Locate and identify every blood parasite.
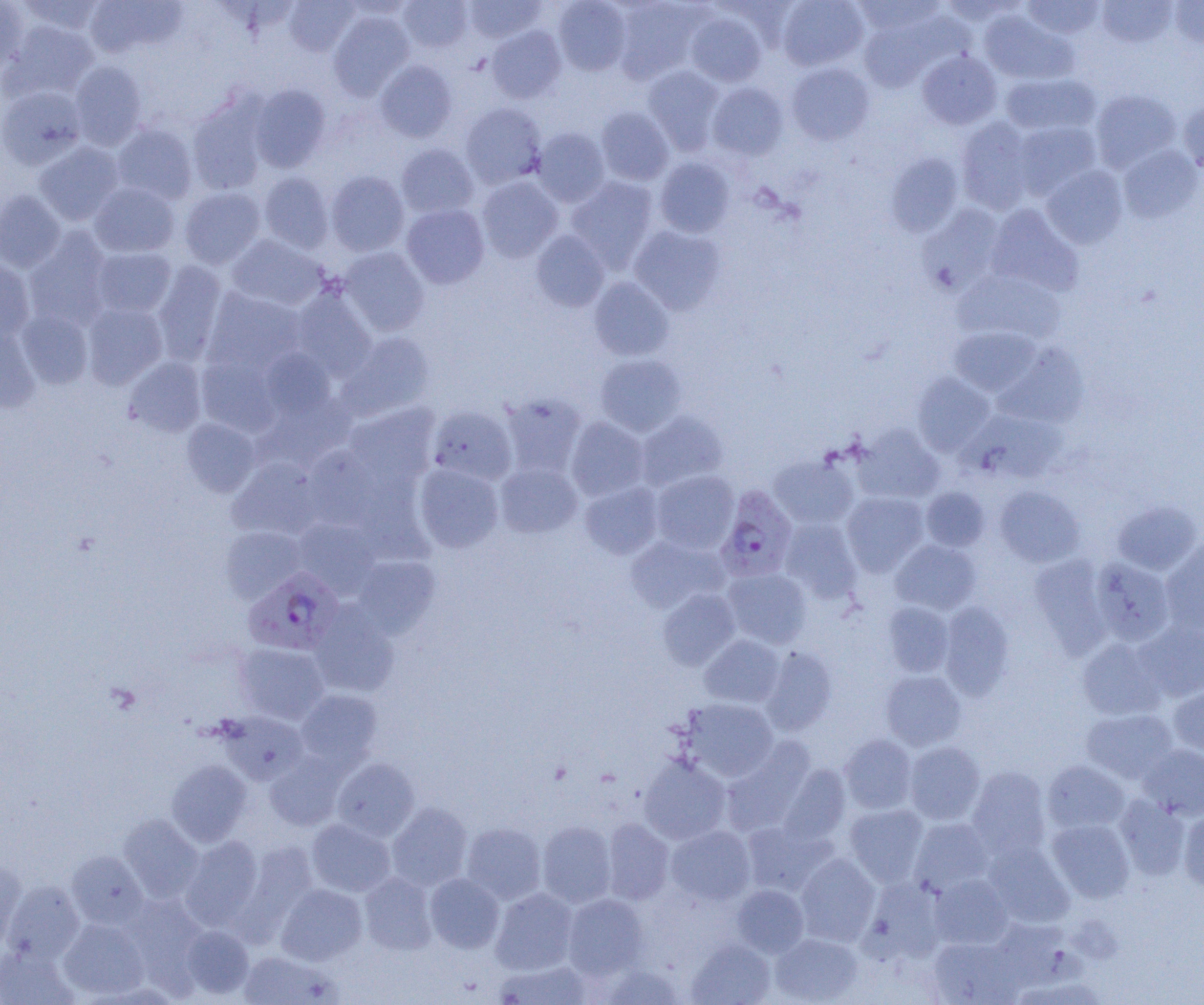

Approximate bounding boxes as (x1, y1, x2, y2) in pixels.
Plasmodium falciparum-infected red blood cells: (715, 485, 798, 582), (244, 567, 344, 654).
No Plasmodium ovale, Plasmodium malariae, Plasmodium vivax, Babesia divergens, or Trypanosoma brucei observed.

Uninfected red blood cell locations: (0, 0, 29, 75), (16, 0, 107, 37), (82, 0, 184, 58), (283, 0, 359, 55), (398, 0, 472, 52), (464, 0, 545, 43), (553, 0, 632, 75), (777, 0, 868, 71), (852, 0, 946, 35), (939, 0, 1025, 26), (1022, 0, 1104, 39), (1097, 0, 1177, 48), (612, 1, 706, 84), (1169, 1, 1204, 47), (685, 10, 767, 87), (329, 11, 414, 99), (979, 11, 1074, 84), (858, 17, 941, 92), (3, 20, 98, 100), (487, 26, 565, 103), (918, 50, 1001, 130), (375, 60, 456, 142), (69, 61, 147, 150), (786, 63, 874, 145), (642, 65, 725, 154), (1001, 72, 1100, 136), (707, 82, 788, 160), (249, 84, 331, 172), (0, 85, 88, 170), (1091, 89, 1181, 172), (188, 98, 269, 194), (1178, 98, 1204, 174), (460, 103, 547, 187), (595, 106, 674, 186), (956, 117, 1035, 215), (1012, 121, 1101, 199), (111, 123, 198, 205), (532, 127, 610, 207), (34, 142, 124, 226), (397, 144, 479, 219), (1118, 145, 1202, 223), (886, 153, 964, 238), (654, 157, 735, 238), (1041, 165, 1128, 249), (326, 171, 409, 256), (259, 172, 334, 253), (476, 176, 563, 262), (565, 176, 659, 271), (90, 182, 179, 258), (180, 186, 265, 269), (0, 190, 66, 272), (401, 204, 489, 289), (919, 204, 1007, 295), (986, 205, 1083, 296), (628, 224, 727, 314), (24, 230, 114, 330), (531, 230, 610, 311), (227, 234, 326, 311), (91, 247, 176, 318), (338, 247, 429, 336), (0, 258, 35, 344), (152, 260, 228, 363), (953, 269, 1065, 345), (589, 277, 674, 361), (290, 286, 377, 379), (203, 288, 304, 375), (82, 302, 168, 388), (16, 309, 93, 388), (948, 325, 1042, 397), (0, 327, 40, 414), (339, 331, 435, 419), (994, 342, 1089, 427), (259, 348, 336, 420), (595, 353, 687, 437), (196, 356, 280, 437), (124, 357, 207, 437), (911, 373, 996, 456), (500, 393, 587, 477), (262, 397, 354, 470), (344, 403, 439, 486), (428, 405, 517, 485), (635, 410, 728, 491), (181, 417, 260, 497), (566, 417, 649, 501), (852, 425, 944, 505), (302, 447, 386, 529), (769, 455, 859, 530), (229, 458, 323, 541), (495, 462, 582, 538), (414, 463, 503, 552), (651, 470, 739, 553), (580, 480, 664, 559), (994, 486, 1085, 567), (921, 487, 990, 551), (841, 491, 929, 576), (1112, 500, 1201, 575), (779, 517, 862, 602), (291, 518, 380, 597), (220, 526, 306, 602), (626, 535, 727, 614), (1162, 537, 1204, 633), (891, 539, 981, 615), (351, 555, 440, 638), (1029, 555, 1113, 656), (1089, 557, 1176, 646), (722, 567, 812, 649), (658, 589, 741, 670), (882, 601, 954, 677), (939, 601, 1015, 699), (308, 603, 399, 698), (1135, 620, 1204, 701), (699, 634, 785, 708), (1077, 637, 1167, 720), (235, 643, 330, 724), (760, 646, 837, 735), (880, 670, 967, 750), (1169, 686, 1204, 756), (295, 689, 382, 769), (680, 697, 778, 781), (1081, 708, 1178, 784), (219, 711, 309, 785), (839, 734, 917, 814), (721, 741, 815, 836), (903, 741, 985, 824), (1138, 744, 1204, 819), (265, 753, 348, 830), (639, 754, 732, 845), (331, 757, 420, 841), (166, 759, 252, 846), (1042, 760, 1129, 835), (778, 764, 851, 844), (966, 767, 1051, 858), (1114, 795, 1190, 880), (387, 802, 472, 891), (845, 803, 929, 886), (1179, 810, 1204, 893), (118, 814, 204, 903), (909, 817, 993, 895), (306, 818, 395, 897), (1047, 818, 1135, 902), (602, 819, 674, 905), (742, 820, 833, 895), (537, 821, 616, 907), (461, 822, 546, 904), (666, 825, 755, 905), (180, 836, 264, 928), (983, 841, 1074, 927), (66, 850, 147, 930), (795, 853, 880, 945), (0, 859, 26, 950), (360, 872, 438, 955), (425, 873, 504, 953), (929, 874, 1012, 949), (862, 877, 947, 963), (4, 880, 85, 963), (276, 884, 367, 965), (732, 884, 808, 957), (491, 888, 578, 974), (563, 894, 648, 978), (58, 918, 149, 999), (181, 926, 254, 998), (770, 933, 862, 1004), (928, 937, 1021, 1004), (687, 939, 775, 1005), (0, 945, 76, 1005), (237, 951, 341, 1004), (493, 959, 591, 1004), (600, 963, 684, 1004). Slide-level diagnosis: Plasmodium falciparum. Image is 1204×1005 pixels. Single field of view. Optical microscopy. 1000x magnification. Thin blood smear.